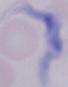

modality: micrograph
magnification: 1000x
identification: trypanosome